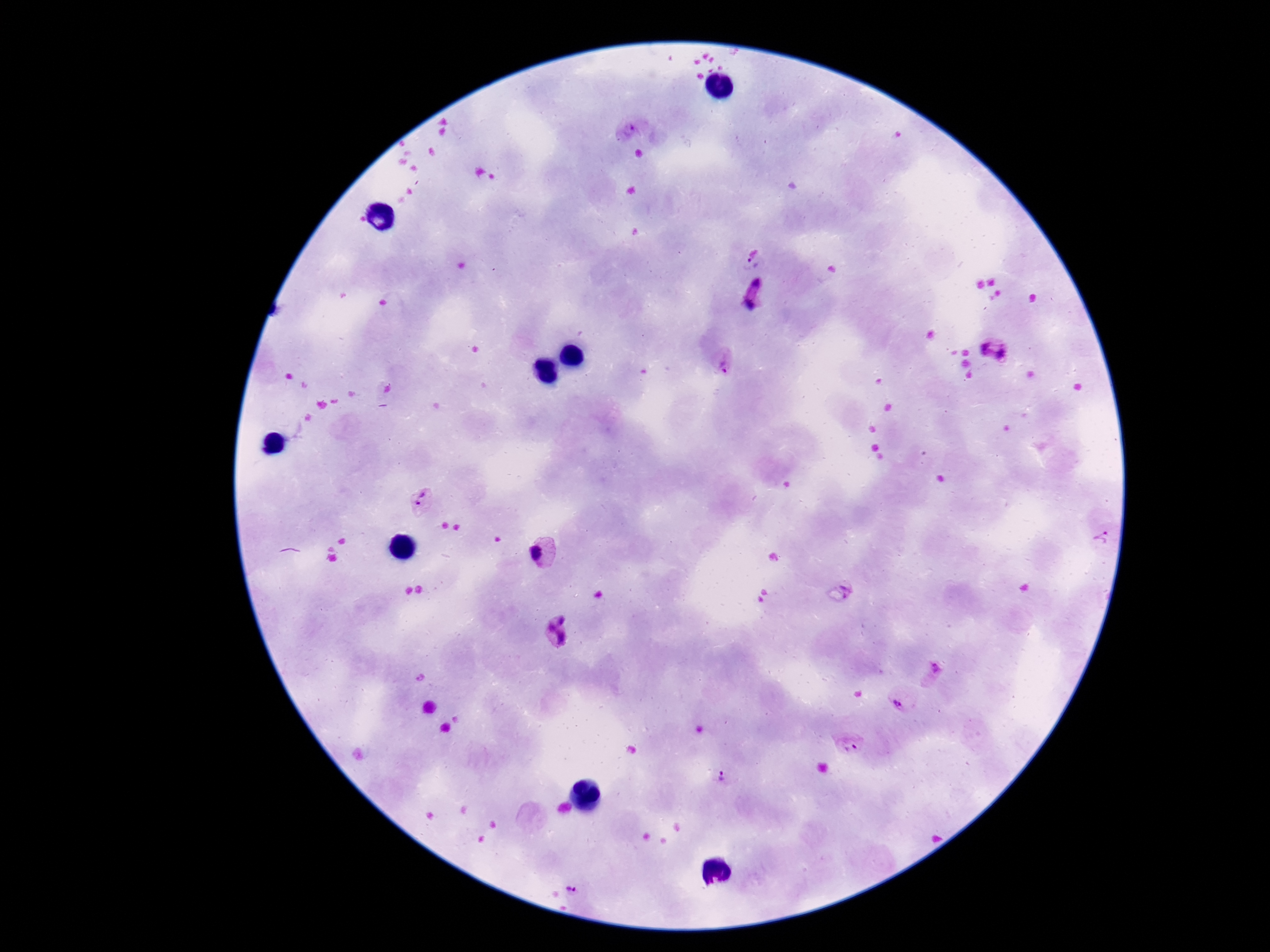
Approximate centers as [x, y] in pixels.
Summary:
  - Plasmodium parasite locations: [632, 129], [754, 255], [754, 295], [994, 353], [722, 363], [420, 502], [1101, 538], [542, 552], [850, 586], [559, 634], [934, 671], [902, 698], [851, 745], [721, 776], [572, 888]
  - Capture: smartphone camera through the microscope eyepiece
  - Stain: Giemsa
  - Patient malaria status: positive
  - Image size: 1270×952 pixels
  - Field of view: one from this slide
  - Preparation: thick blood smear
  - Magnification: 100x